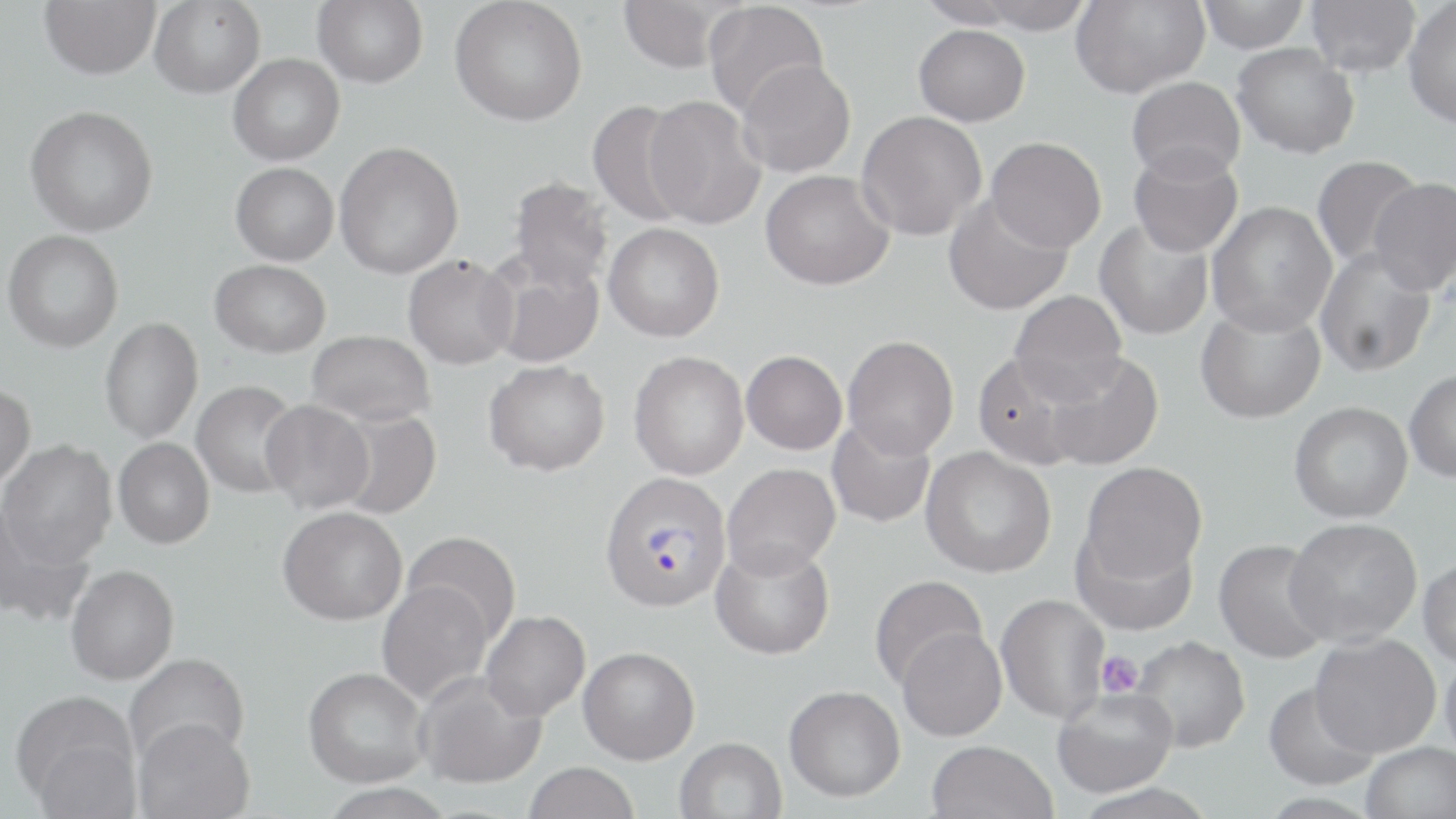

Approximate bounding boxes as (x1, y1, x2, y2) in pixels. Plasmodium vivax-infected red blood cell locations: (599, 473, 732, 613). Platelet locations: (1096, 651, 1143, 697). Uninfected red blood cell locations: (39, 0, 160, 79), (150, 0, 265, 98), (312, 0, 428, 88), (450, 0, 587, 126), (616, 0, 734, 72), (916, 0, 1027, 29), (971, 0, 1096, 34), (1070, 0, 1209, 99), (1196, 0, 1310, 53), (1305, 0, 1421, 77), (1403, 1, 1456, 128), (703, 2, 829, 119), (913, 24, 1030, 126), (1232, 43, 1360, 158), (228, 54, 344, 165), (736, 59, 856, 177), (1127, 77, 1245, 182), (643, 95, 767, 230), (587, 99, 696, 227), (25, 105, 158, 237), (856, 111, 987, 240), (986, 136, 1107, 252), (334, 141, 464, 279), (1128, 144, 1243, 257), (1311, 155, 1426, 271), (230, 162, 338, 265), (760, 170, 894, 290), (507, 177, 614, 294), (1368, 177, 1456, 296), (943, 194, 1072, 317), (1206, 201, 1337, 337), (1094, 218, 1214, 340), (603, 222, 724, 342), (2, 230, 123, 353), (1315, 247, 1437, 378), (485, 254, 604, 369), (402, 255, 518, 370), (210, 259, 330, 358), (1009, 291, 1128, 404), (1196, 301, 1326, 424), (99, 318, 204, 443), (306, 330, 435, 425), (842, 335, 959, 458), (741, 350, 847, 455), (1041, 350, 1164, 471), (628, 351, 749, 480), (972, 351, 1092, 471), (483, 360, 610, 476), (1404, 369, 1456, 483), (191, 380, 302, 499), (0, 383, 35, 490), (260, 400, 375, 514), (1289, 400, 1413, 523), (331, 409, 441, 519), (827, 417, 936, 528), (113, 437, 214, 549), (0, 440, 117, 567), (921, 447, 1057, 578), (1079, 461, 1208, 585), (722, 462, 841, 578), (0, 503, 94, 628), (278, 506, 407, 625), (1285, 517, 1422, 647), (1071, 523, 1199, 636), (402, 531, 521, 646), (1213, 538, 1334, 664), (710, 540, 834, 660), (1418, 557, 1456, 668), (66, 564, 179, 685), (869, 574, 988, 690), (376, 579, 494, 704), (996, 594, 1110, 723), (480, 610, 590, 721), (897, 627, 1007, 742), (1310, 633, 1441, 757), (1129, 635, 1251, 753), (578, 646, 700, 764), (1439, 648, 1456, 767), (124, 653, 250, 767), (303, 666, 430, 788), (414, 671, 546, 788), (1264, 681, 1380, 791), (784, 685, 906, 802), (1052, 687, 1178, 797), (12, 692, 141, 812), (133, 718, 255, 818), (673, 737, 787, 819), (925, 739, 1057, 819), (1362, 742, 1455, 819), (523, 762, 639, 819), (319, 784, 456, 818). Slide-level diagnosis: Plasmodium vivax. Thin blood smear. One field of a larger specimen. May-Grünwald-Giemsa stain. Captured at 1000x magnification. Light microscopy. Image is 1456×819 pixels.